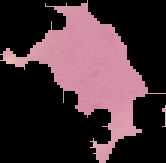
From a thin blood film. Malaria status: uninfected. Image is 166×163 pixels. Segmented cell region on a black background.